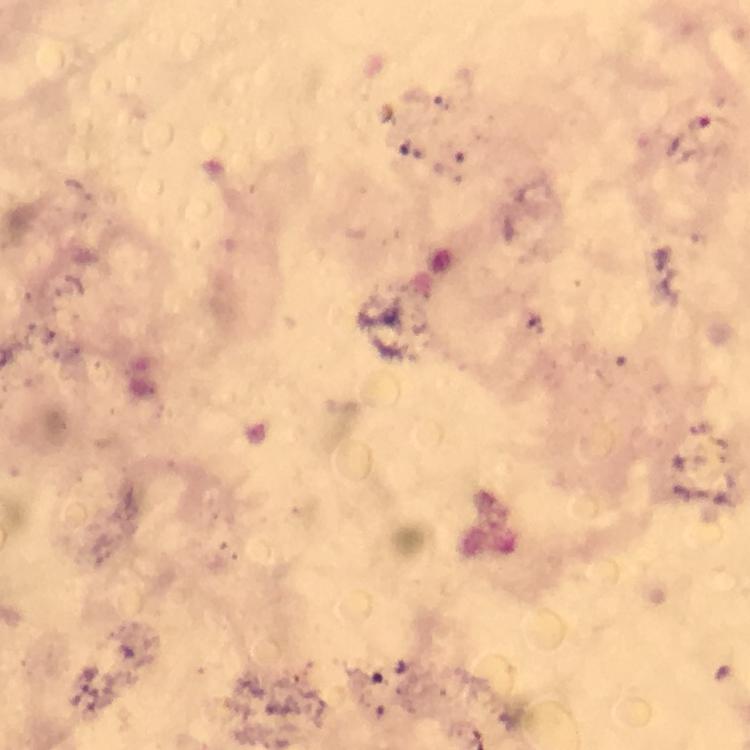

Approximate centers as [x, y] in pixels. Malaria parasite locations: [699, 125]. Giemsa-stained preparation. Thick smear. 100x magnification. Photographed with a smartphone mounted on the microscope. Immersion oil applied. Cropped region of a single field of view. Image is 750×750 pixels. From a diagnostic examination for malaria.